Locate every leukocyte (white blood cell).
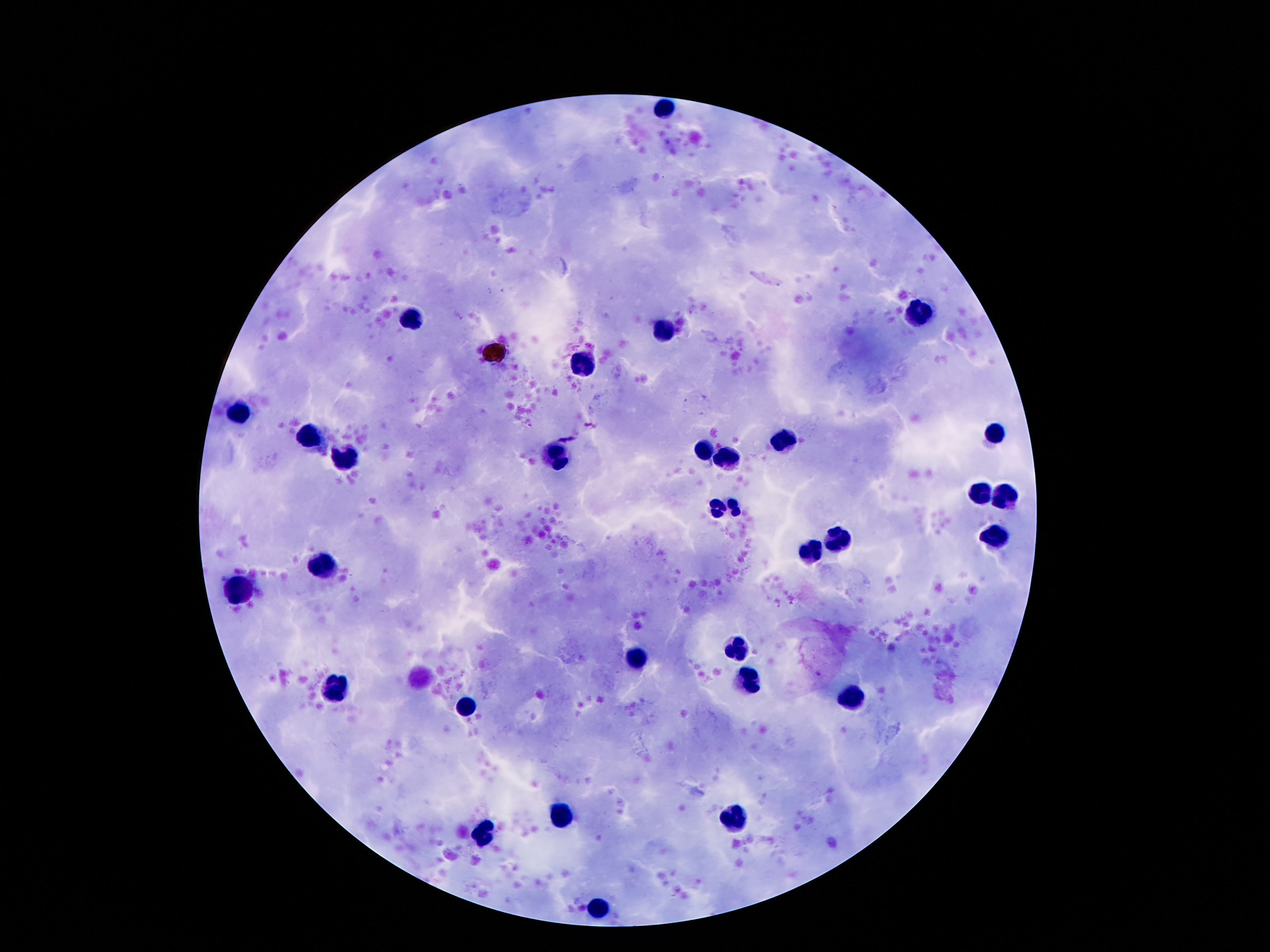
Approximate centers as [x, y] in pixels.
Leukocytes: [666, 107], [922, 311], [409, 318], [664, 332], [581, 363], [241, 412], [996, 432], [306, 438], [782, 442], [702, 451], [555, 457], [728, 458], [345, 460], [980, 489], [1008, 493], [726, 508], [988, 531], [840, 537], [810, 552], [322, 562], [241, 591], [736, 649], [637, 659], [752, 683], [338, 690], [850, 700], [466, 705], [563, 814], [734, 819], [487, 831], [600, 910].

{
  "magnification": "100x",
  "image_size": "1270×952 pixels",
  "patient_malaria_status": "not infected",
  "field_of_view": "one from this slide",
  "capture": "smartphone camera through the microscope eyepiece",
  "preparation": "thick blood film",
  "stain": "Giemsa"
}